Outline each blood parasite and name the species.
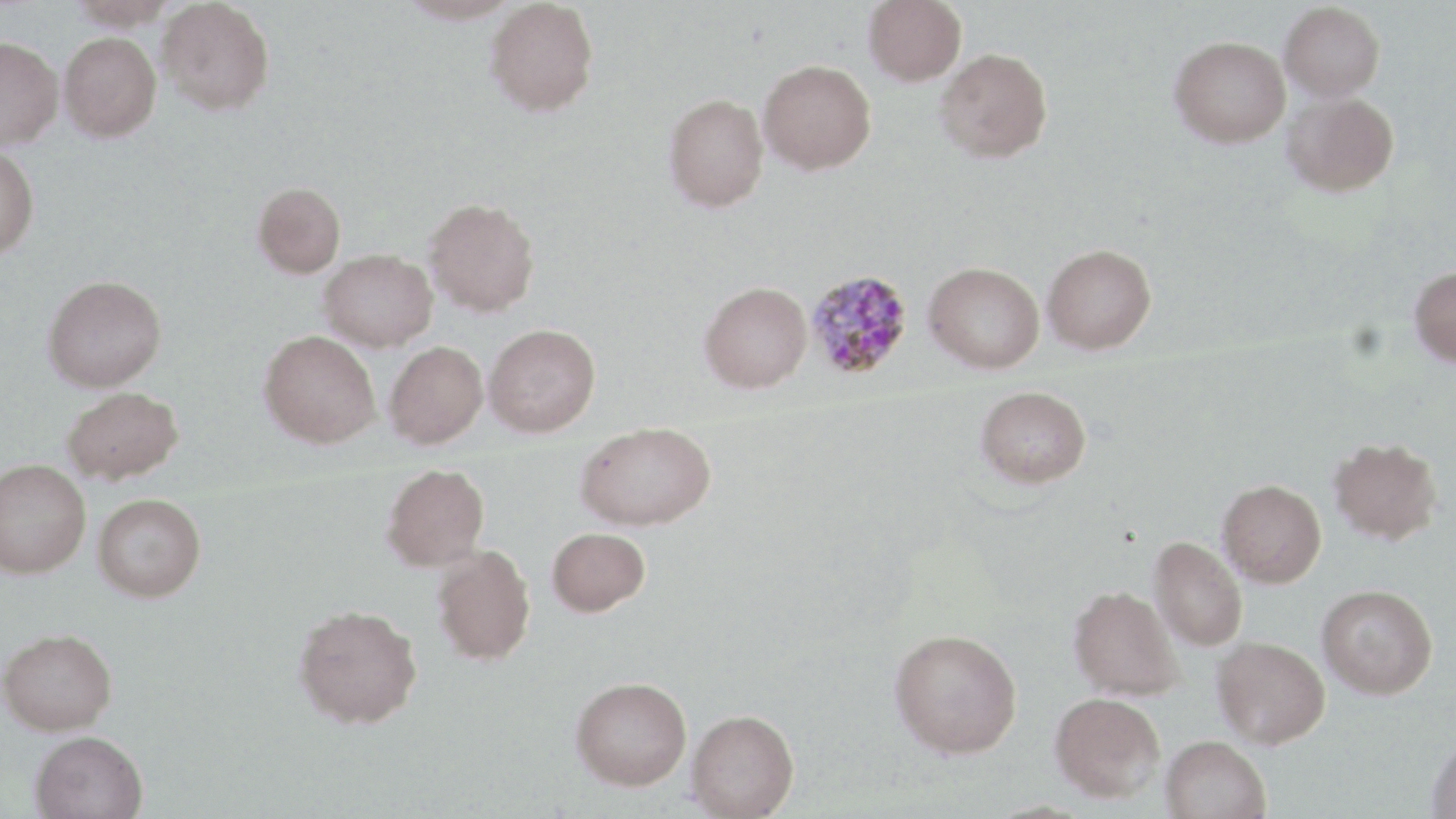

Approximate bounding boxes as (x1,y1)-(x2,y2) corner pairs in pixels.
Plasmodium malariae-infected red blood cells: (804,268)-(914,380).
No Plasmodium falciparum, Plasmodium ovale, Plasmodium vivax, Babesia divergens, or Trypanosoma brucei observed.

Summary:
  - Uninfected red blood cell locations: (65,0)-(182,30), (157,0)-(275,115), (397,0)-(522,25), (485,0)-(599,117), (863,0)-(967,87), (1280,2)-(1384,101), (59,32)-(161,142), (0,35)-(63,151), (1170,35)-(1290,147), (935,47)-(1052,163), (758,59)-(876,174), (1282,92)-(1399,197), (663,93)-(769,212), (0,145)-(39,259), (252,181)-(346,278), (424,197)-(540,317), (1042,243)-(1156,354), (319,249)-(437,351), (924,261)-(1044,373), (1408,266)-(1456,367), (42,275)-(166,392), (699,281)-(812,393), (484,324)-(600,438), (259,330)-(380,448), (384,341)-(488,448), (976,385)-(1091,488), (62,386)-(184,484), (575,421)-(716,531), (1328,437)-(1443,544), (0,458)-(90,578), (382,463)-(490,571), (1217,479)-(1327,588), (93,493)-(206,602), (547,527)-(650,616), (1149,536)-(1247,651), (432,543)-(536,665), (1317,584)-(1438,699), (1068,585)-(1184,701), (292,603)-(423,729), (889,627)-(1022,758), (0,628)-(117,735), (1212,636)-(1330,748), (571,676)-(691,789), (1050,692)-(1165,802), (687,708)-(799,818), (29,730)-(148,819), (1426,734)-(1456,818), (1161,735)-(1271,819)
  - Slide-level diagnosis: Plasmodium malariae
  - Field of view: single
  - Stain: May-Grünwald-Giemsa
  - Preparation: thin blood film
  - Image size: 1456×819 pixels
  - Magnification: 1000x
  - Modality: optical microscopy